Comment on the morphology of the red blood cells.
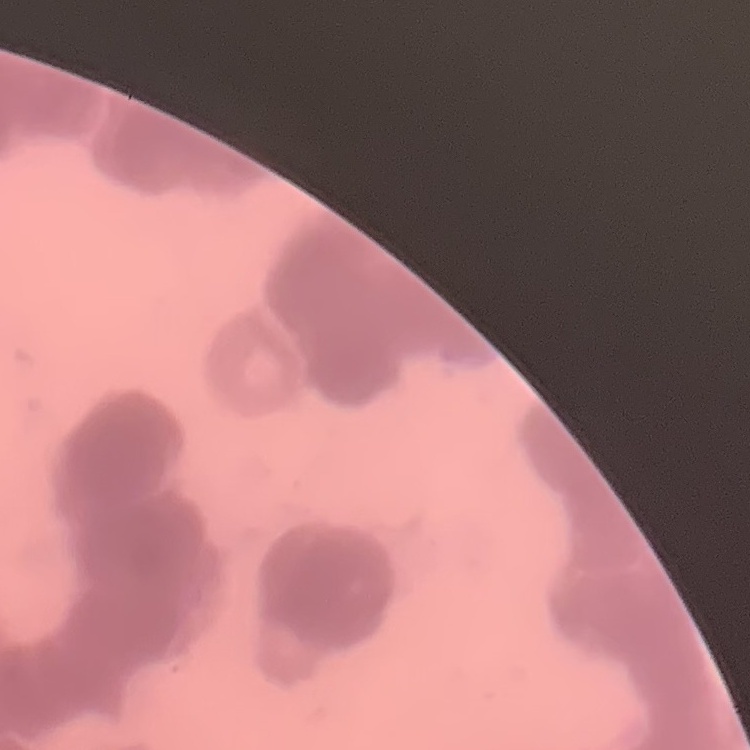
They show rouleaux formation.

One tile cut from a larger photomicrograph. Field's or Giemsa stain. Thin peripheral smear.